Assess for Plasmodium parasites.
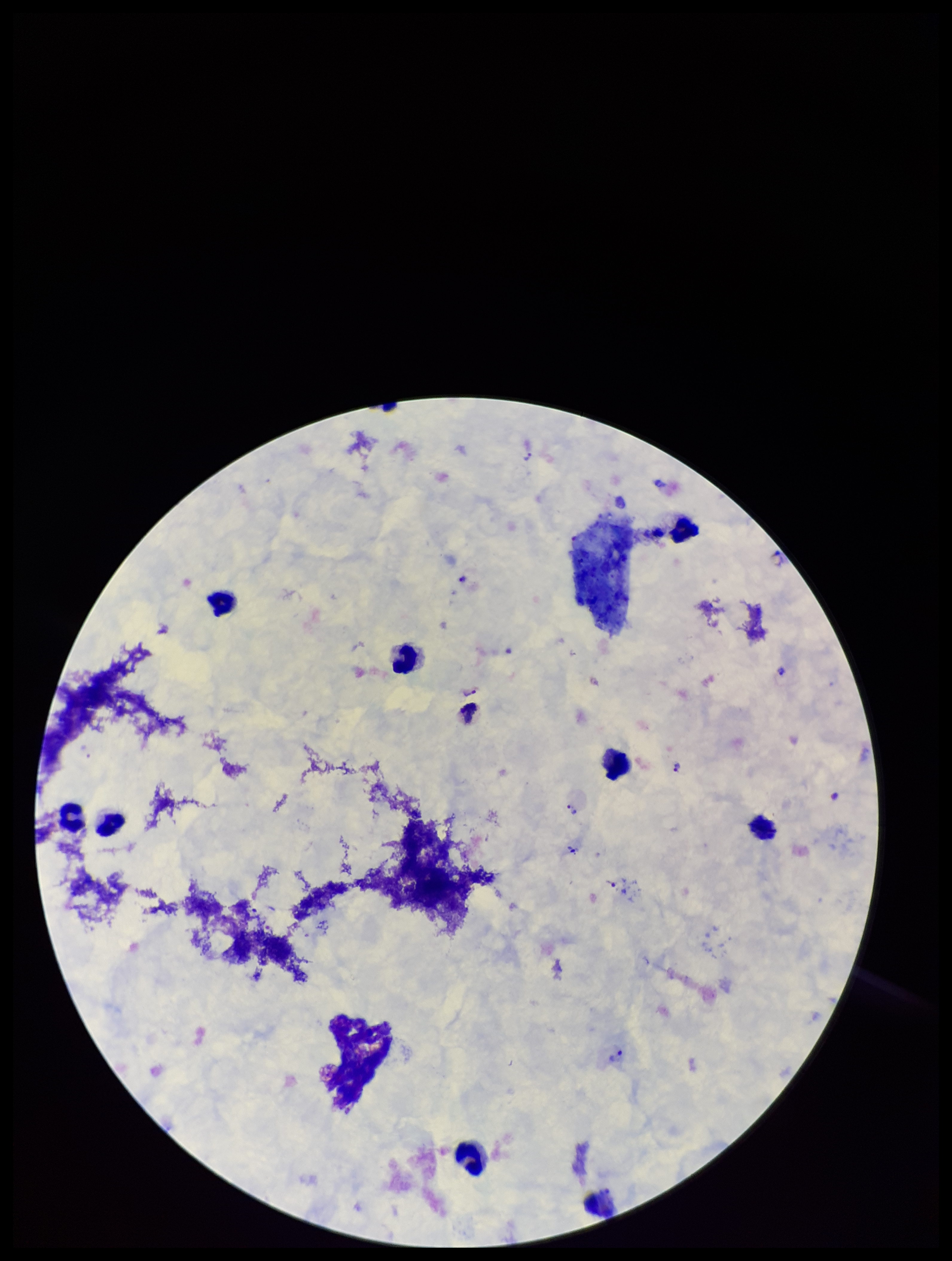

Identified.

Smartphone photograph taken through the eyepiece of a microscope. One field from this slide. Giemsa stain. Parasite count: 7. Leukocyte count: 9. Patient malaria status: positive. Preparation: thick. Image is 952×1261 pixels. Species reported for this patient: Plasmodium vivax.